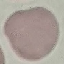

Result: no malaria parasites detected. Thin blood film. Giemsa stain. Automatically extracted cell patch, resized to 64 × 64 pixels. Photographed with a smartphone camera at the microscope eyepiece.